Assess this cell for malaria.
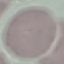
Uninfected.

Thin blood smear. Photographed with a smartphone camera at the microscope eyepiece. Giemsa-stained preparation. Automatically extracted cell patch, resized to 64 × 64 pixels.